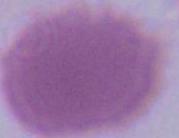 Captured at 1000x magnification. An erythrocyte is shown. Photomicrograph.